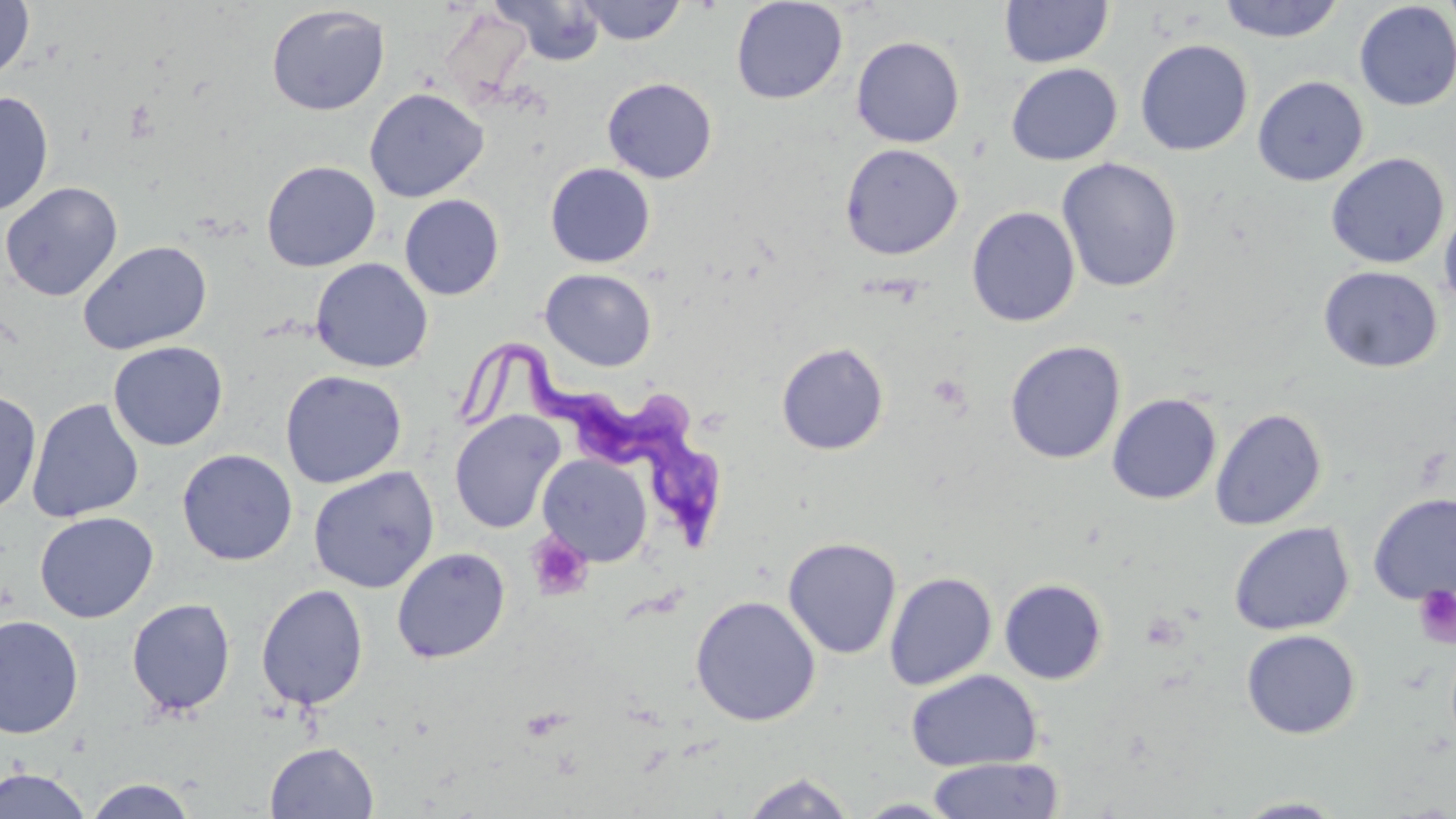

slide-level diagnosis = Trypanosoma brucei
magnification = 1000x
field of view = single
Trypanosoma brucei locations = approximate bounding boxes as named x1/y1/x2/y2 corners in pixels: (x1=467, y1=344, x2=725, y2=549)
uninfected red blood cell locations = approximate bounding boxes as named x1/y1/x2/y2 corners in pixels: (x1=493, y1=0, x2=606, y2=67), (x1=576, y1=0, x2=688, y2=45), (x1=731, y1=0, x2=848, y2=104), (x1=1217, y1=0, x2=1346, y2=43), (x1=1440, y1=0, x2=1456, y2=39), (x1=0, y1=1, x2=35, y2=82), (x1=999, y1=1, x2=1114, y2=68), (x1=1354, y1=2, x2=1456, y2=112), (x1=266, y1=4, x2=390, y2=116), (x1=437, y1=9, x2=535, y2=106), (x1=851, y1=36, x2=965, y2=148), (x1=1134, y1=39, x2=1254, y2=156), (x1=1005, y1=63, x2=1123, y2=166), (x1=1252, y1=75, x2=1369, y2=187), (x1=602, y1=77, x2=718, y2=184), (x1=363, y1=87, x2=489, y2=203), (x1=0, y1=91, x2=54, y2=218), (x1=839, y1=143, x2=963, y2=260), (x1=1326, y1=152, x2=1449, y2=269), (x1=1057, y1=157, x2=1183, y2=293), (x1=261, y1=160, x2=381, y2=271), (x1=544, y1=162, x2=656, y2=268), (x1=0, y1=181, x2=123, y2=301), (x1=398, y1=194, x2=505, y2=300), (x1=1439, y1=202, x2=1456, y2=315), (x1=966, y1=206, x2=1081, y2=327), (x1=78, y1=239, x2=213, y2=355), (x1=310, y1=257, x2=433, y2=373), (x1=1318, y1=265, x2=1443, y2=373), (x1=540, y1=268, x2=657, y2=371), (x1=1004, y1=340, x2=1126, y2=464), (x1=108, y1=341, x2=228, y2=451), (x1=775, y1=342, x2=890, y2=455), (x1=279, y1=369, x2=407, y2=488), (x1=0, y1=389, x2=42, y2=517), (x1=1106, y1=393, x2=1222, y2=505), (x1=27, y1=398, x2=144, y2=522), (x1=1210, y1=407, x2=1328, y2=531), (x1=449, y1=410, x2=566, y2=534), (x1=176, y1=448, x2=298, y2=566), (x1=537, y1=454, x2=653, y2=567), (x1=307, y1=465, x2=440, y2=593), (x1=1367, y1=492, x2=1456, y2=605), (x1=34, y1=511, x2=158, y2=623), (x1=1228, y1=521, x2=1355, y2=635), (x1=783, y1=536, x2=902, y2=660), (x1=391, y1=547, x2=510, y2=664), (x1=884, y1=571, x2=998, y2=690), (x1=998, y1=578, x2=1108, y2=684), (x1=256, y1=584, x2=369, y2=711), (x1=690, y1=594, x2=821, y2=726), (x1=126, y1=598, x2=236, y2=717), (x1=0, y1=614, x2=84, y2=740), (x1=1241, y1=629, x2=1361, y2=740), (x1=905, y1=669, x2=1043, y2=771), (x1=265, y1=741, x2=379, y2=819), (x1=926, y1=756, x2=1064, y2=818), (x1=1, y1=766, x2=91, y2=819), (x1=739, y1=771, x2=858, y2=819), (x1=83, y1=778, x2=199, y2=819), (x1=1232, y1=796, x2=1348, y2=817), (x1=851, y1=798, x2=961, y2=818)
platelet locations = approximate bounding boxes as named x1/y1/x2/y2 corners in pixels: (x1=527, y1=533, x2=594, y2=601), (x1=1412, y1=585, x2=1456, y2=649)
preparation = thin blood smear
image size = 1456×819 pixels
modality = light microscopy
stain = May-Grünwald-Giemsa